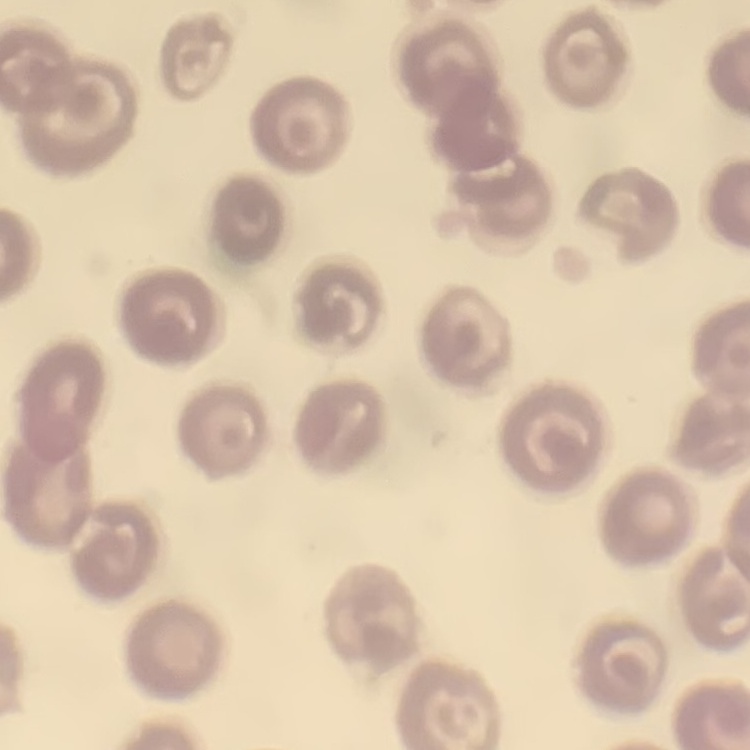
Summary:
  - Erythrocyte morphology: no rouleaux formation
  - Preparation: thin blood film
  - Stain: Field's or Giemsa
  - Image type: square crop of a larger photomicrograph